Outline each Plasmodium falciparum-infected red blood cell.
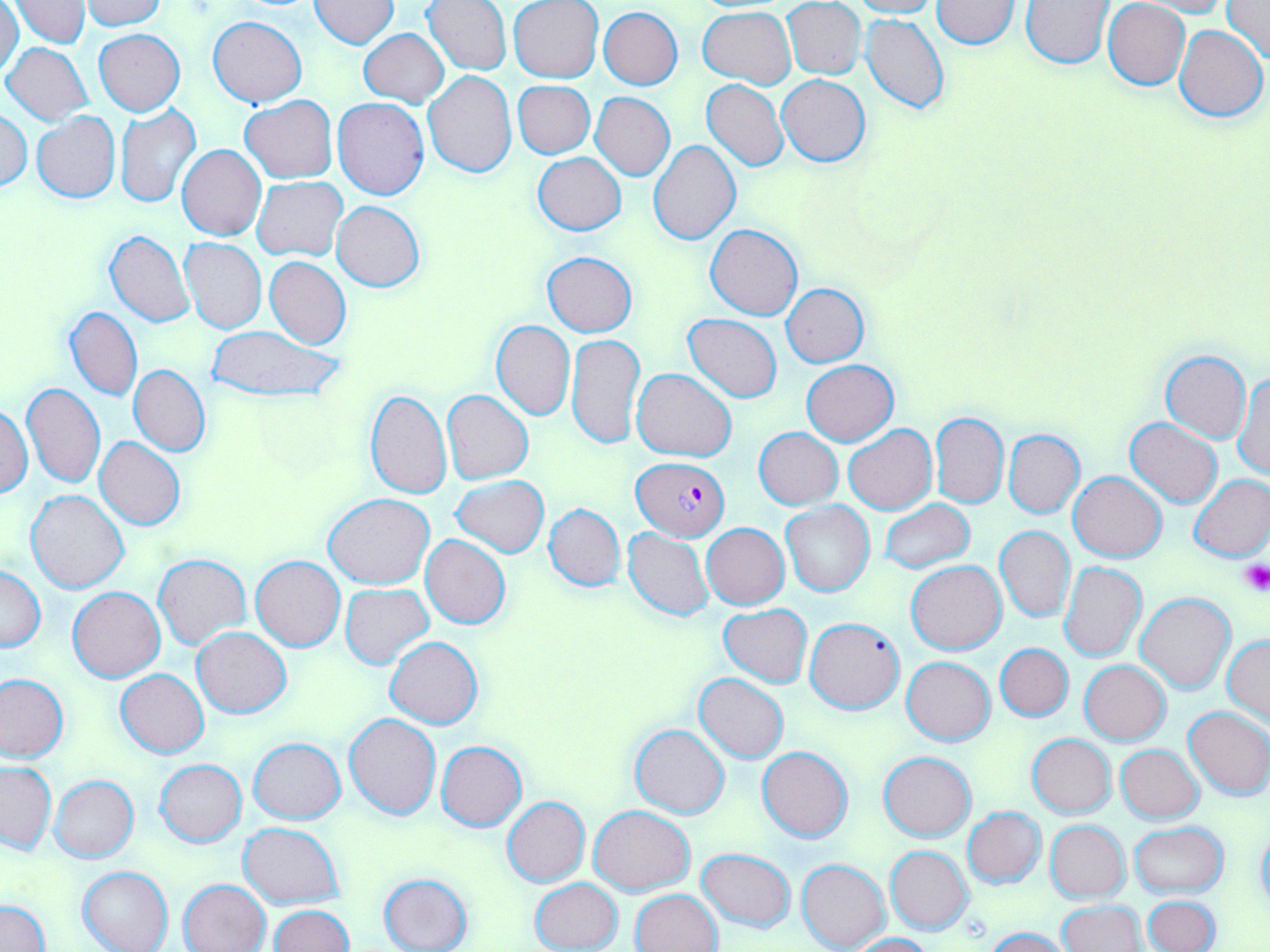

Approximate bounding boxes as [x1, y1, x2, y2] in pixels.
Plasmodium falciparum-infected red blood cells: [632, 456, 728, 540].

{
  "slide_level_diagnosis": "Plasmodium falciparum",
  "magnification": "1000x",
  "image_size": "1270×952 pixels",
  "preparation": "thin blood film",
  "platelet_locations": "approximate bounding boxes as [x1, y1, x2, y2] in pixels: [1237, 559, 1269, 596]",
  "uninfected_red_blood_cell_locations": "approximate bounding boxes as [x1, y1, x2, y2] in pixels: [80, 0, 168, 30], [309, 0, 398, 48], [847, 0, 939, 19], [1021, 0, 1114, 68], [1103, 0, 1191, 89], [0, 1, 22, 81], [11, 1, 88, 48], [423, 1, 511, 74], [508, 1, 604, 83], [783, 1, 866, 80], [929, 1, 1021, 49], [1135, 1, 1229, 18], [1220, 1, 1270, 64], [598, 6, 683, 89], [699, 7, 796, 87], [861, 13, 949, 115], [209, 15, 306, 106], [1173, 25, 1268, 123], [358, 27, 447, 107], [94, 30, 185, 116], [3, 43, 94, 127], [423, 70, 517, 177], [777, 75, 869, 167], [701, 80, 788, 171], [512, 81, 595, 159], [591, 92, 674, 180], [240, 95, 337, 183], [334, 97, 430, 200], [115, 103, 201, 208], [1, 108, 32, 190], [32, 112, 120, 202], [648, 141, 741, 246], [177, 144, 266, 241], [534, 151, 625, 235], [252, 178, 347, 260], [332, 201, 424, 292], [706, 224, 803, 321], [104, 230, 195, 328], [180, 237, 267, 334], [542, 252, 637, 336], [265, 256, 350, 350], [781, 283, 870, 368], [65, 307, 143, 401], [683, 314, 782, 403], [490, 320, 576, 420], [205, 326, 343, 405], [567, 333, 644, 449], [1161, 350, 1252, 442], [801, 360, 899, 445], [129, 365, 210, 455], [632, 369, 737, 461], [1234, 369, 1269, 479], [20, 382, 105, 488], [365, 389, 450, 498], [442, 390, 533, 484], [0, 402, 33, 499], [930, 412, 1008, 509], [1124, 418, 1222, 507], [844, 425, 937, 515], [753, 427, 842, 510], [1003, 430, 1084, 517], [95, 437, 186, 530], [1068, 471, 1166, 562], [1189, 474, 1270, 563], [453, 476, 549, 556], [26, 490, 129, 593], [324, 493, 435, 589], [880, 500, 973, 572], [782, 502, 874, 597], [544, 503, 624, 592], [701, 523, 790, 610], [995, 526, 1075, 623], [622, 527, 714, 621], [421, 534, 510, 629], [153, 555, 250, 648], [251, 556, 345, 651], [906, 561, 1006, 655], [1059, 562, 1147, 662], [0, 566, 45, 651], [340, 584, 432, 668], [68, 586, 165, 682], [1135, 592, 1236, 694], [718, 604, 811, 687], [804, 617, 905, 713], [192, 627, 291, 718], [386, 635, 482, 729], [1223, 636, 1269, 726], [995, 642, 1074, 722], [901, 656, 996, 745], [1079, 660, 1170, 745], [116, 669, 208, 758], [0, 674, 68, 762], [694, 674, 789, 763], [1184, 705, 1270, 800], [344, 714, 441, 819], [629, 724, 729, 819], [1026, 733, 1116, 818], [249, 738, 345, 823], [437, 741, 527, 831], [1116, 745, 1205, 823], [757, 746, 853, 842], [879, 752, 976, 840], [155, 758, 247, 847], [0, 762, 57, 854], [50, 775, 139, 864], [502, 796, 589, 886], [590, 805, 693, 895], [962, 807, 1046, 888], [1045, 820, 1130, 903], [1128, 820, 1229, 899], [238, 822, 345, 910], [885, 846, 974, 934], [696, 847, 796, 932], [797, 858, 889, 951], [77, 866, 173, 952], [378, 873, 472, 952], [180, 878, 271, 952], [531, 878, 621, 951], [631, 889, 722, 952], [1143, 895, 1219, 952], [1, 899, 49, 952], [1058, 902, 1146, 952], [271, 906, 354, 952], [984, 927, 1070, 952], [847, 933, 935, 952]",
  "field_of_view": "one of a larger specimen",
  "modality": "light microscopy",
  "stain": "May-Grünwald-Giemsa"
}